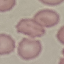 Result: no malaria parasites seen. Giemsa stain. Acquired by smartphone through the microscope eyepiece. Thin blood smear. Cell patch, automatically extracted from a larger field of view and resized to 64 × 64 pixels.